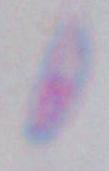

magnification: 1000x
modality: micrograph
identification: Toxoplasma gondii